Report the malaria status of this cell.
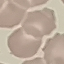
Uninfected.

Giemsa-stained preparation. Photographed with a smartphone camera at the microscope eyepiece. Cell patch, automatically extracted from a larger field of view and resized to 64 × 64 pixels. Thin blood film.